State the blood parasite species.
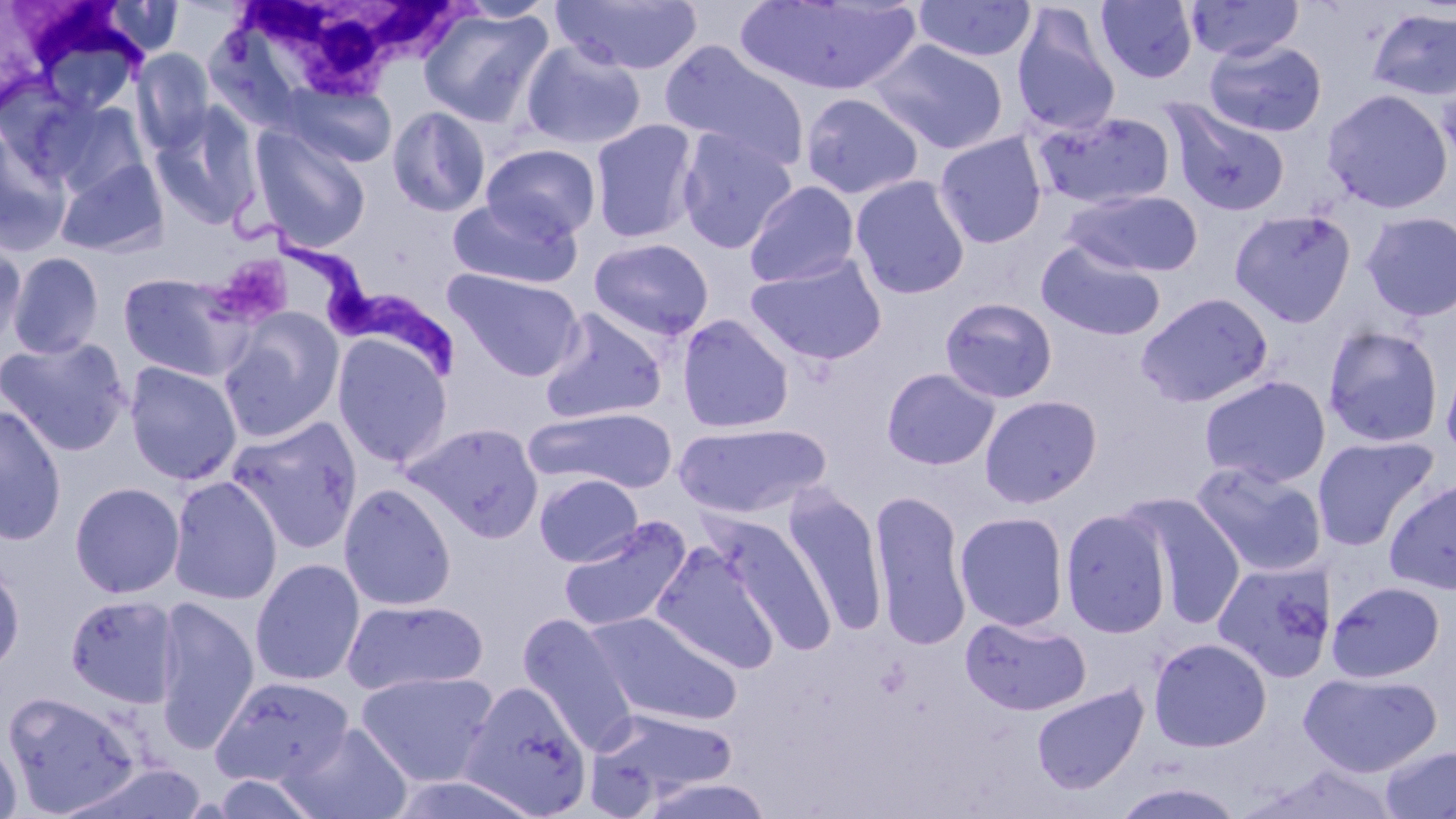

Trypanosoma brucei.

magnification = 1000x
modality = optical microscopy
platelet locations = approximate bounding boxes as [x1, y1, x2, y2] in pixels: [222, 255, 294, 320]
image size = 1456×819 pixels
Trypanosoma brucei locations = approximate bounding boxes as [x1, y1, x2, y2] in pixels: [235, 190, 462, 375]
uninfected red blood cell locations (subset) = approximate bounding boxes as [x1, y1, x2, y2] in pixels: [551, 0, 703, 76], [734, 0, 921, 97], [1186, 0, 1304, 62], [100, 1, 185, 57], [912, 1, 1037, 63], [1096, 1, 1198, 84], [418, 6, 555, 128], [1366, 7, 1456, 101], [1011, 8, 1121, 137], [1204, 38, 1327, 138], [869, 39, 1010, 154], [520, 40, 647, 151], [660, 41, 811, 172], [131, 48, 215, 153], [1437, 72, 1456, 172], [282, 82, 397, 168], [1321, 88, 1453, 214], [799, 92, 924, 200], [37, 97, 151, 200], [1163, 98, 1290, 217], [150, 106, 264, 230], [387, 106, 491, 217], [1033, 110, 1176, 210], [590, 119, 700, 245], [250, 125, 372, 252], [677, 129, 797, 253], [934, 132, 1047, 249], [0, 134, 70, 254], [481, 143, 601, 241], [54, 158, 170, 258], [850, 175, 970, 299], [743, 181, 860, 287], [1062, 189, 1203, 277], [447, 196, 581, 290], [1229, 208, 1356, 327], [1360, 211, 1456, 321], [0, 235, 28, 352], [589, 237, 714, 341], [1036, 239, 1165, 341], [6, 251, 104, 360], [746, 254, 887, 365], [444, 268, 585, 381], [116, 272, 253, 381], [1136, 292, 1274, 408], [939, 297, 1058, 403], [539, 307, 669, 425], [218, 311, 344, 441], [677, 314, 794, 433], [1322, 325, 1444, 448], [0, 335, 132, 457], [332, 335, 453, 467], [1440, 347, 1456, 467], [124, 361, 242, 485], [881, 368, 1000, 470], [1199, 375, 1331, 488], [979, 394, 1102, 508], [0, 405, 67, 545], [525, 406, 678, 492], [225, 416, 364, 554], [402, 421, 544, 541], [674, 422, 830, 519], [1312, 435, 1440, 551], [1190, 461, 1328, 578], [534, 473, 643, 567], [167, 475, 283, 606], [1384, 477, 1456, 595], [69, 481, 185, 598], [339, 482, 457, 612], [781, 489, 888, 635], [869, 489, 972, 651], [1124, 493, 1248, 627], [1060, 508, 1172, 638], [955, 511, 1069, 631], [709, 513, 839, 655], [557, 515, 692, 634], [651, 542, 781, 673], [250, 557, 365, 687], [0, 560, 25, 677], [1213, 560, 1337, 683], [1326, 580, 1447, 683], [64, 593, 181, 709], [153, 595, 260, 752], [342, 598, 488, 695], [587, 611, 742, 728], [518, 614, 638, 753], [961, 614, 1092, 716], [1148, 637, 1272, 752], [355, 670, 499, 787], [1299, 670, 1442, 778], [211, 675, 354, 787], [459, 681, 593, 818], [1031, 684, 1148, 794], [3, 690, 143, 816], [588, 709, 739, 809], [283, 722, 413, 819], [0, 734, 23, 819], [1380, 745, 1456, 819], [208, 772, 321, 818], [635, 776, 777, 819], [1109, 781, 1247, 819]
white blood cell locations (subset) = approximate bounding boxes as [x1, y1, x2, y2] in pixels: [232, 0, 471, 101]
field of view = one of a larger specimen
stain = May-Grünwald-Giemsa
preparation = thin blood film